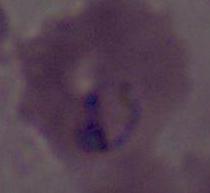

Summary:
  - Modality: micrograph
  - Magnification: 400x or 1000x
  - Identification: Plasmodium